Assess this cell for malaria.
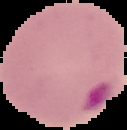

It is parasitized.

preparation = thin blood film
image type = cell region segmented out of the field of view; surrounding area masked to black
image size = 127×130 pixels